Classify this cell by malaria status.
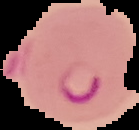
It is parasitized.

Image is 139×130 pixels. Cell region segmented out of the field of view; the surrounding area is masked to black. From a thin blood film.